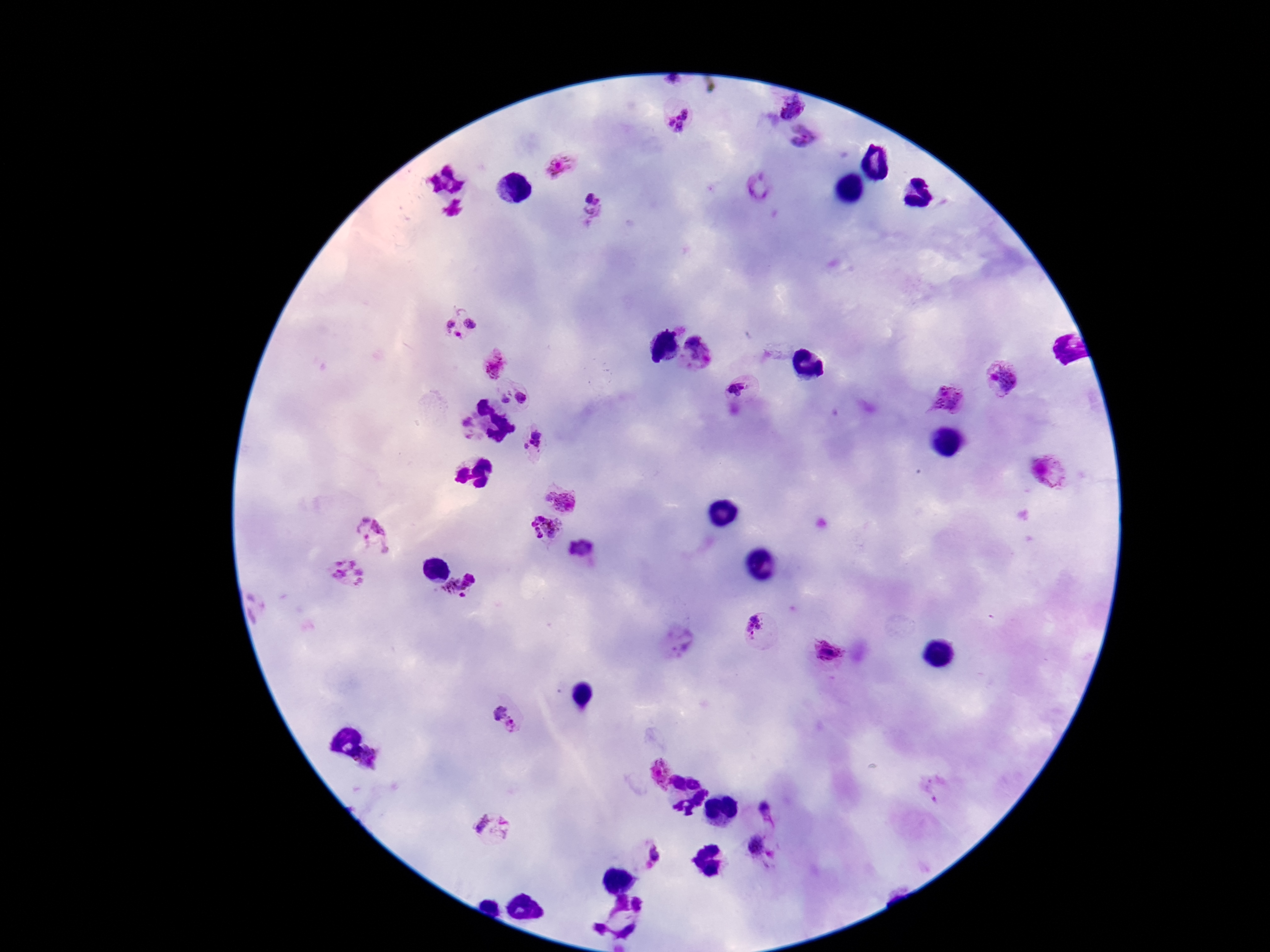

Approximate object centers, in pixels from the top-left corner. Plasmodium parasite locations: (x=676, y=78), (x=791, y=107), (x=678, y=119), (x=803, y=137), (x=558, y=166), (x=759, y=190), (x=591, y=211), (x=459, y=324), (x=696, y=354), (x=1006, y=381), (x=736, y=392), (x=526, y=394), (x=506, y=396), (x=949, y=400), (x=469, y=428), (x=530, y=441), (x=1047, y=473), (x=560, y=502), (x=545, y=529), (x=372, y=533), (x=583, y=547), (x=345, y=575), (x=462, y=590), (x=757, y=630), (x=673, y=644), (x=827, y=651), (x=508, y=717), (x=372, y=762), (x=658, y=772), (x=768, y=811), (x=493, y=828), (x=756, y=847), (x=646, y=855). Patient malaria status: infected. Image is 1270×952 pixels. Thick peripheral-blood smear. One field from this slide. 100x magnification. Photographed through the microscope eyepiece with a smartphone camera. Giemsa stain.